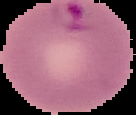 From a thin blood film. Malaria status: parasitized. Segmented cell region on a black background. Image is 136×115 pixels.